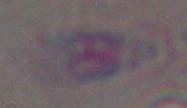 Toxoplasma gondii is seen. 1000x magnification. Micrograph.